Assess the morphology of the erythrocytes.
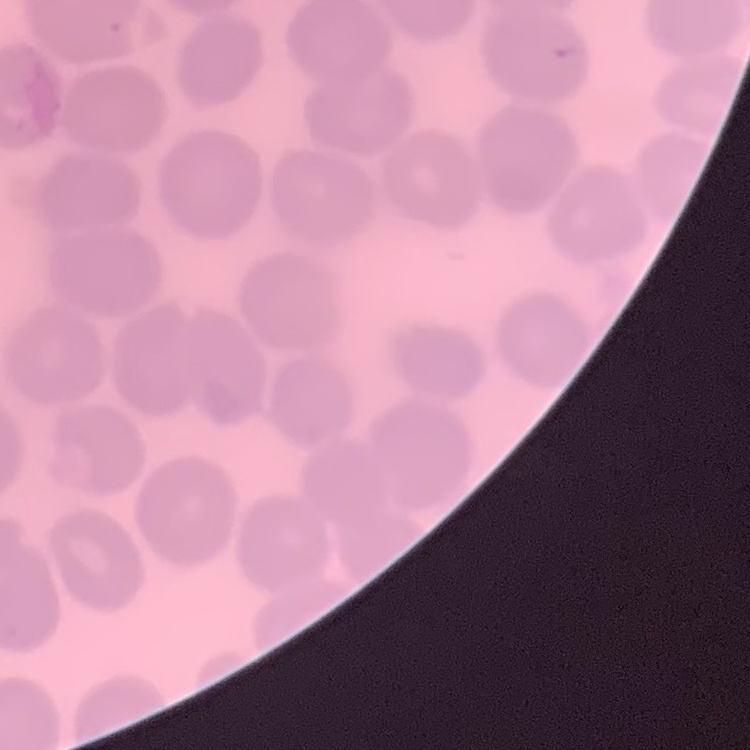

They show no rouleaux formation.

Square crop of a larger photomicrograph. Field's or Giemsa stain. Thin blood film.